Describe the morphology of the erythrocytes.
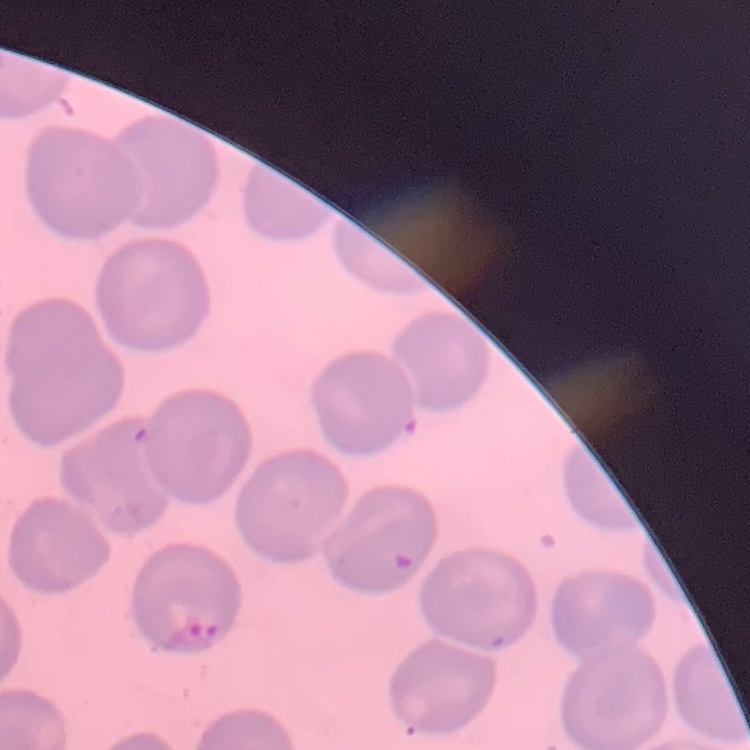

No rouleaux formation.

Summary:
  - Image type: one tile cut from a larger photomicrograph
  - Stain: Field's or Giemsa
  - Preparation: thin peripheral smear